Locate every malaria parasite.
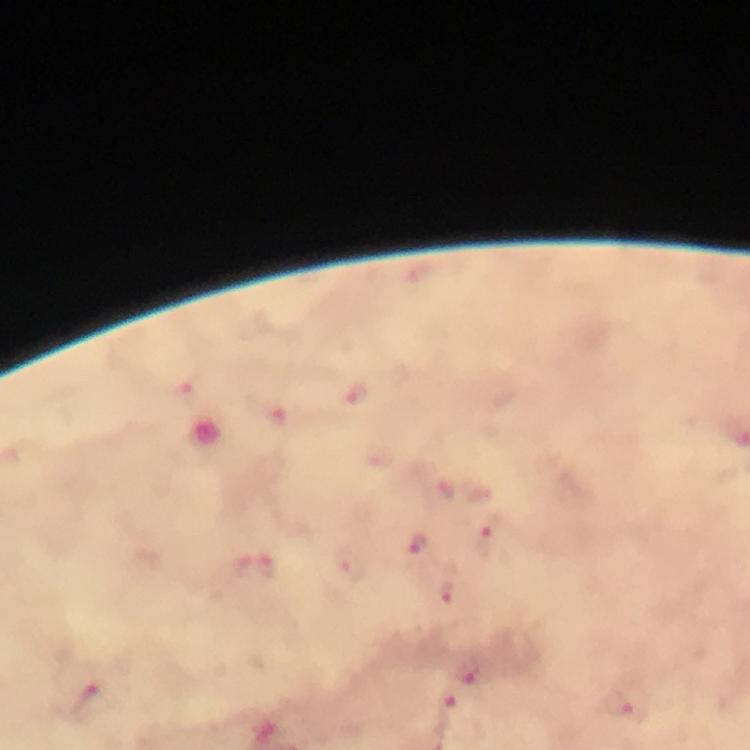

Approximate object centers, in pixels from the top-left corner.
Malaria parasites: (x=356, y=393), (x=190, y=394), (x=443, y=486), (x=492, y=539), (x=419, y=543), (x=349, y=565), (x=268, y=566), (x=454, y=585), (x=470, y=670), (x=617, y=701), (x=92, y=704).

Giemsa-stained preparation. Thick blood film. Immersion oil was used. A crop from one field of view. Image is 750×750 pixels. From a diagnostic examination for malaria. Photographed through the microscope with a smartphone camera. 100x magnification.